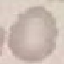

malaria status = uninfected
stain = Giemsa
capture = smartphone through the microscope eyepiece
preparation = thin smear
image type = cell patch, automatically extracted from a larger field of view and resized to 64 × 64 pixels